State the blood parasite species.
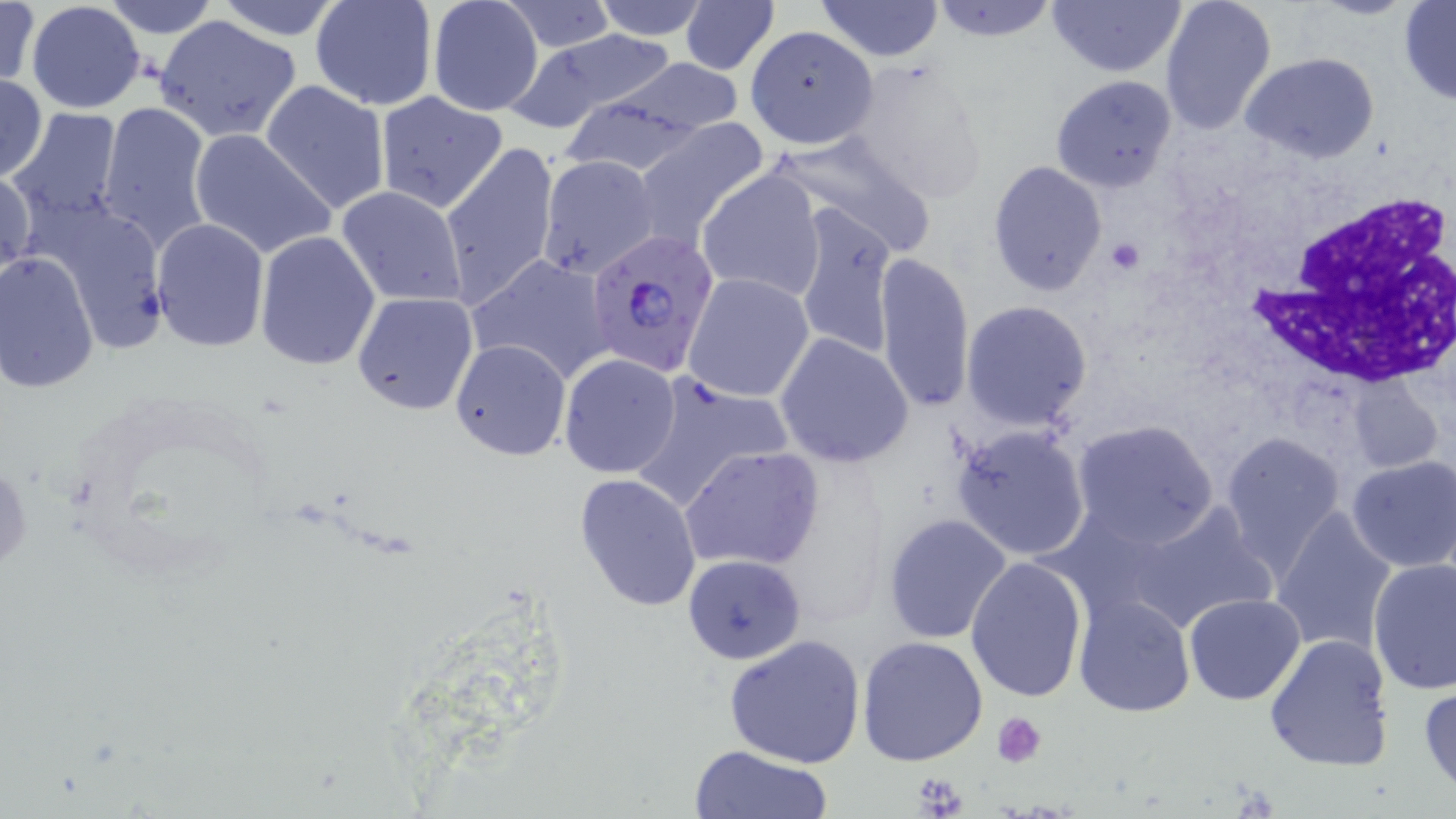

Plasmodium falciparum.

Summary:
  - Coordinate format: approximate bounding boxes as named x1/y1/x2/y2 corners in pixels
  - Plasmodium falciparum-infected red blood cell locations: (x1=583, y1=234, x2=716, y2=380)
  - Uninfected red blood cell locations: (x1=0, y1=0, x2=40, y2=93), (x1=98, y1=0, x2=221, y2=40), (x1=310, y1=0, x2=437, y2=111), (x1=426, y1=0, x2=545, y2=118), (x1=585, y1=0, x2=714, y2=39), (x1=814, y1=0, x2=944, y2=63), (x1=1046, y1=0, x2=1187, y2=79), (x1=1159, y1=0, x2=1278, y2=134), (x1=1398, y1=0, x2=1456, y2=104), (x1=927, y1=1, x2=1062, y2=45), (x1=25, y1=2, x2=146, y2=114), (x1=208, y1=2, x2=350, y2=41), (x1=497, y1=2, x2=619, y2=53), (x1=679, y1=2, x2=779, y2=75), (x1=153, y1=15, x2=302, y2=142), (x1=744, y1=30, x2=881, y2=150), (x1=508, y1=32, x2=682, y2=132), (x1=1241, y1=54, x2=1380, y2=165), (x1=841, y1=56, x2=992, y2=204), (x1=608, y1=57, x2=747, y2=137), (x1=0, y1=73, x2=47, y2=183), (x1=1049, y1=74, x2=1179, y2=194), (x1=260, y1=80, x2=391, y2=216), (x1=375, y1=91, x2=508, y2=213), (x1=554, y1=94, x2=709, y2=176), (x1=98, y1=101, x2=214, y2=251), (x1=8, y1=109, x2=124, y2=234), (x1=630, y1=117, x2=770, y2=247), (x1=188, y1=127, x2=335, y2=260), (x1=769, y1=131, x2=939, y2=259), (x1=440, y1=141, x2=560, y2=308), (x1=988, y1=161, x2=1108, y2=299), (x1=1, y1=163, x2=34, y2=288), (x1=697, y1=167, x2=827, y2=303), (x1=337, y1=185, x2=468, y2=308), (x1=34, y1=199, x2=168, y2=358), (x1=790, y1=203, x2=900, y2=362), (x1=150, y1=218, x2=270, y2=353), (x1=254, y1=231, x2=381, y2=370), (x1=0, y1=250, x2=99, y2=396), (x1=874, y1=252, x2=976, y2=414), (x1=466, y1=255, x2=615, y2=386), (x1=683, y1=273, x2=814, y2=402), (x1=353, y1=292, x2=480, y2=415), (x1=960, y1=300, x2=1093, y2=432), (x1=774, y1=332, x2=916, y2=468), (x1=450, y1=337, x2=572, y2=461), (x1=558, y1=354, x2=682, y2=479), (x1=626, y1=372, x2=793, y2=513), (x1=1343, y1=372, x2=1445, y2=478), (x1=1071, y1=419, x2=1219, y2=547), (x1=950, y1=424, x2=1091, y2=562), (x1=1220, y1=429, x2=1347, y2=576), (x1=680, y1=446, x2=825, y2=571), (x1=1346, y1=456, x2=1456, y2=572), (x1=575, y1=473, x2=702, y2=613), (x1=1114, y1=498, x2=1280, y2=634), (x1=1270, y1=506, x2=1400, y2=657), (x1=882, y1=513, x2=1013, y2=646), (x1=683, y1=555, x2=806, y2=665), (x1=1367, y1=556, x2=1455, y2=695), (x1=966, y1=557, x2=1089, y2=705), (x1=1073, y1=593, x2=1195, y2=717), (x1=1184, y1=593, x2=1306, y2=705), (x1=721, y1=633, x2=867, y2=769), (x1=1263, y1=633, x2=1394, y2=772), (x1=856, y1=636, x2=989, y2=767), (x1=1417, y1=684, x2=1456, y2=794), (x1=686, y1=745, x2=833, y2=819)
  - White blood cell locations: (x1=1256, y1=190, x2=1456, y2=387)
  - Platelet locations: (x1=1104, y1=236, x2=1148, y2=275), (x1=990, y1=710, x2=1047, y2=766), (x1=907, y1=770, x2=970, y2=819)
  - Stain: May-Grünwald-Giemsa
  - Modality: light microscopy
  - Magnification: 1000x
  - Preparation: thin blood smear
  - Image size: 1456×819 pixels
  - Field of view: one of a larger specimen